State which parasite is depicted.
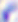
This is Toxoplasma gondii.

modality = photomicrograph
magnification = 400x